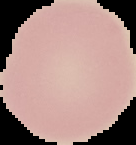 Malaria status: uninfected. Cell region segmented out of the field of view; the surrounding area is masked to black. From a thin blood film. Image is 136×145 pixels.